State which parasite is depicted.
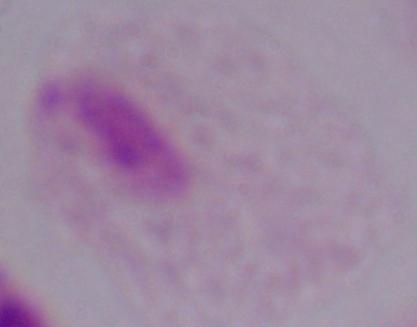
A trichomonad.

Summary:
  - Magnification: 1000x
  - Modality: photomicrograph